Mark where platelets are.
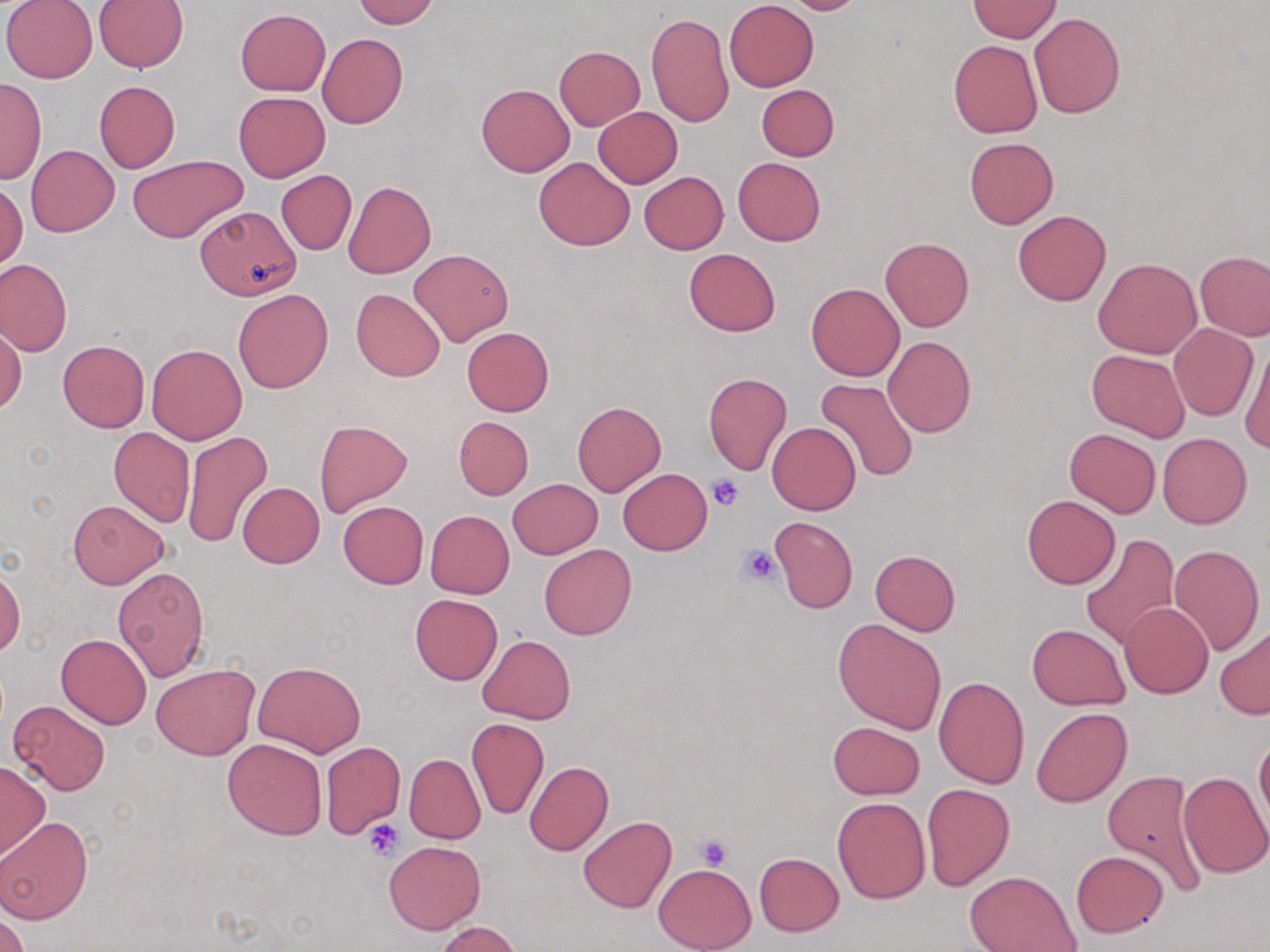
Approximate bounding boxes as (x1,y1)-(x2,y2) corner pairs in pixels.
Platelets: (710,475)-(743,510), (738,543)-(782,589), (362,817)-(404,858), (694,834)-(733,871).

Uninfected red blood cell locations: (2,0)-(97,83), (351,0)-(438,27), (777,0)-(868,15), (93,1)-(189,73), (724,1)-(819,91), (968,1)-(1061,41), (234,8)-(331,96), (1029,12)-(1126,118), (646,13)-(733,126), (317,34)-(408,129), (947,40)-(1043,138), (553,46)-(645,130), (0,78)-(46,185), (94,81)-(180,172), (477,83)-(574,176), (756,84)-(839,160), (233,91)-(331,183), (593,107)-(683,187), (963,137)-(1059,229), (26,145)-(119,237), (127,154)-(248,243), (533,157)-(635,249), (733,157)-(825,246), (276,170)-(356,255), (638,172)-(729,254), (343,180)-(435,279), (0,182)-(25,272), (195,205)-(302,297), (1014,210)-(1110,305), (880,237)-(974,332), (409,247)-(513,346), (685,247)-(781,336), (1196,250)-(1270,340), (0,258)-(73,358), (1093,258)-(1201,358), (806,282)-(904,381), (351,288)-(445,381), (233,289)-(333,394), (1168,323)-(1257,420), (1,324)-(24,415), (462,327)-(554,416), (884,336)-(975,436), (58,339)-(149,432), (147,344)-(247,444), (1240,345)-(1269,453), (1087,348)-(1190,442), (703,372)-(792,475), (814,377)-(920,485), (573,400)-(665,496), (453,416)-(534,499), (313,420)-(413,518), (767,423)-(860,515), (108,428)-(194,527), (180,428)-(275,547), (1064,429)-(1161,517), (1157,431)-(1253,528), (617,468)-(713,555), (508,478)-(603,559), (238,483)-(324,568), (1021,494)-(1120,588), (68,500)-(168,588), (338,501)-(429,588), (425,510)-(516,599), (769,517)-(859,613), (1081,534)-(1180,649), (539,544)-(637,640), (1168,545)-(1265,656), (870,549)-(960,636), (0,565)-(23,658), (113,566)-(209,680), (411,594)-(502,685), (1119,602)-(1213,698), (833,617)-(948,734), (1028,625)-(1129,708), (1215,626)-(1270,718), (56,633)-(152,729), (478,634)-(575,724), (253,661)-(366,756), (152,663)-(259,761), (932,675)-(1030,789), (8,700)-(111,796), (1031,708)-(1132,807), (466,718)-(550,820), (828,721)-(924,799), (1255,735)-(1270,829), (223,739)-(327,839), (319,742)-(405,838), (404,752)-(485,844), (0,760)-(51,858), (524,761)-(613,856), (1102,769)-(1208,896), (1177,771)-(1270,878), (922,783)-(1015,890), (832,797)-(930,903), (579,815)-(676,913), (0,816)-(93,923), (384,841)-(486,934), (1070,850)-(1167,938), (754,852)-(844,936), (653,864)-(756,951), (965,871)-(1081,952), (0,911)-(29,952), (433,922)-(523,952). Slide-level diagnosis: no evidence of blood parasites. One field of a larger specimen. Captured at 1000x magnification. May-Grünwald-Giemsa-stained preparation. Optical microscopy. Image is 1270×952 pixels. Thin blood smear.